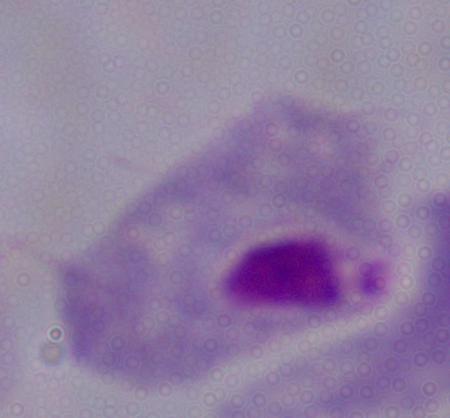
Summary:
  - Magnification: 1000x
  - Modality: photomicrograph
  - Identification: trichomonad